Classify this cell by malaria status.
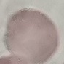
It is uninfected.

stain = Giemsa
image type = automatically extracted cell patch, resized to 64 × 64 pixels
capture = smartphone camera at the microscope eyepiece
preparation = thin blood smear